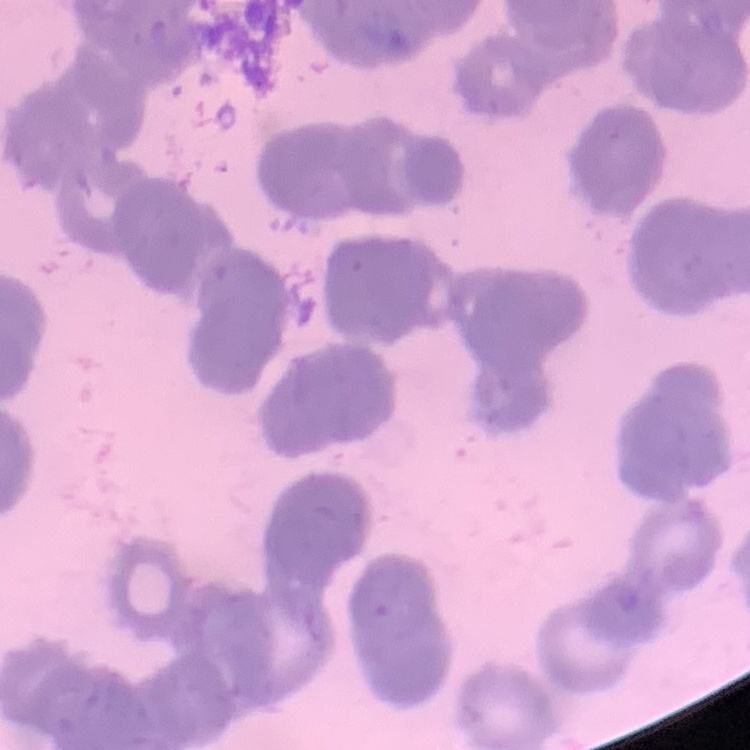
Summary:
  - Erythrocyte morphology: rouleaux formation
  - Image type: square crop of a larger photomicrograph
  - Preparation: thin blood smear
  - Stain: Field's or Giemsa